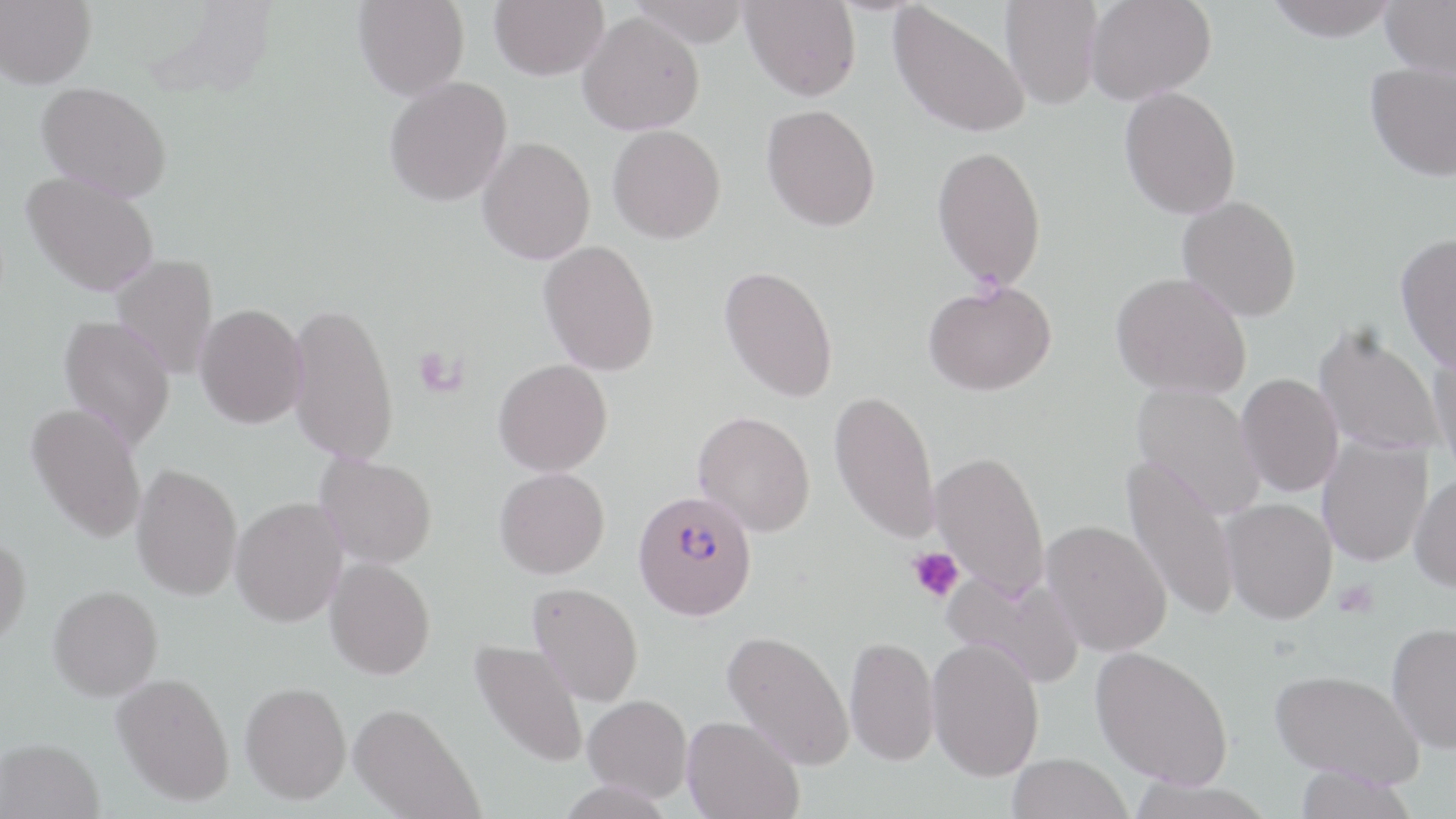 Approximate bounding boxes as named x1/y1/x2/y2 corners in pixels. Plasmodium falciparum-infected red blood cell locations: (x1=633, y1=491, x2=758, y2=619). Uninfected red blood cell locations: (x1=0, y1=0, x2=96, y2=89), (x1=353, y1=0, x2=470, y2=100), (x1=489, y1=0, x2=609, y2=80), (x1=628, y1=0, x2=752, y2=47), (x1=741, y1=0, x2=861, y2=101), (x1=1000, y1=0, x2=1104, y2=109), (x1=1086, y1=0, x2=1216, y2=103), (x1=1266, y1=0, x2=1400, y2=41), (x1=1379, y1=0, x2=1456, y2=77), (x1=888, y1=1, x2=1030, y2=139), (x1=578, y1=12, x2=705, y2=135), (x1=1365, y1=61, x2=1456, y2=182), (x1=384, y1=76, x2=512, y2=206), (x1=36, y1=81, x2=173, y2=203), (x1=1119, y1=85, x2=1242, y2=219), (x1=761, y1=104, x2=881, y2=231), (x1=608, y1=125, x2=726, y2=243), (x1=477, y1=136, x2=596, y2=264), (x1=931, y1=144, x2=1047, y2=290), (x1=22, y1=171, x2=159, y2=296), (x1=1177, y1=195, x2=1302, y2=321), (x1=1395, y1=232, x2=1456, y2=375), (x1=538, y1=240, x2=660, y2=375), (x1=111, y1=254, x2=218, y2=380), (x1=719, y1=264, x2=838, y2=403), (x1=1111, y1=272, x2=1251, y2=400), (x1=923, y1=280, x2=1057, y2=395), (x1=286, y1=300, x2=399, y2=465), (x1=195, y1=304, x2=307, y2=429), (x1=58, y1=315, x2=176, y2=450), (x1=1313, y1=325, x2=1445, y2=456), (x1=1429, y1=349, x2=1456, y2=485), (x1=493, y1=359, x2=612, y2=476), (x1=1236, y1=373, x2=1344, y2=497), (x1=1130, y1=384, x2=1266, y2=521), (x1=829, y1=389, x2=941, y2=544), (x1=26, y1=402, x2=147, y2=543), (x1=693, y1=410, x2=815, y2=536), (x1=1317, y1=435, x2=1433, y2=567), (x1=930, y1=449, x2=1049, y2=599), (x1=315, y1=454, x2=437, y2=568), (x1=1121, y1=455, x2=1241, y2=624), (x1=132, y1=463, x2=243, y2=600), (x1=494, y1=467, x2=609, y2=579), (x1=1410, y1=473, x2=1456, y2=591), (x1=230, y1=497, x2=348, y2=626), (x1=1220, y1=498, x2=1338, y2=624), (x1=1042, y1=520, x2=1172, y2=657), (x1=0, y1=534, x2=31, y2=651), (x1=325, y1=558, x2=435, y2=679), (x1=942, y1=570, x2=1085, y2=687), (x1=528, y1=582, x2=644, y2=706), (x1=48, y1=584, x2=163, y2=700), (x1=1386, y1=621, x2=1456, y2=753), (x1=722, y1=630, x2=854, y2=770), (x1=844, y1=635, x2=939, y2=766), (x1=927, y1=637, x2=1044, y2=781), (x1=470, y1=639, x2=589, y2=769), (x1=1090, y1=646, x2=1233, y2=789), (x1=1270, y1=668, x2=1424, y2=788), (x1=112, y1=672, x2=235, y2=805), (x1=240, y1=681, x2=351, y2=804), (x1=583, y1=694, x2=692, y2=801), (x1=348, y1=702, x2=484, y2=819), (x1=682, y1=715, x2=804, y2=819), (x1=0, y1=738, x2=104, y2=819), (x1=1008, y1=753, x2=1132, y2=819), (x1=1292, y1=765, x2=1418, y2=818), (x1=1124, y1=778, x2=1277, y2=818). Platelet locations: (x1=413, y1=346, x2=466, y2=396), (x1=908, y1=546, x2=964, y2=605). Slide-level diagnosis: Plasmodium falciparum. Thin blood film. Image is 1456×819 pixels. May-Grünwald-Giemsa stain. Optical microscopy. One field of a larger specimen. 1000x magnification.